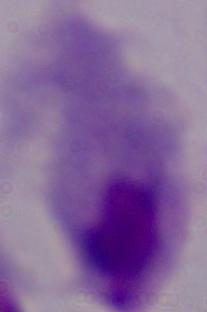

Summary:
  - Modality: photomicrograph
  - Identification: trichomonad
  - Magnification: 1000x